Outline each uninfected red blood cell.
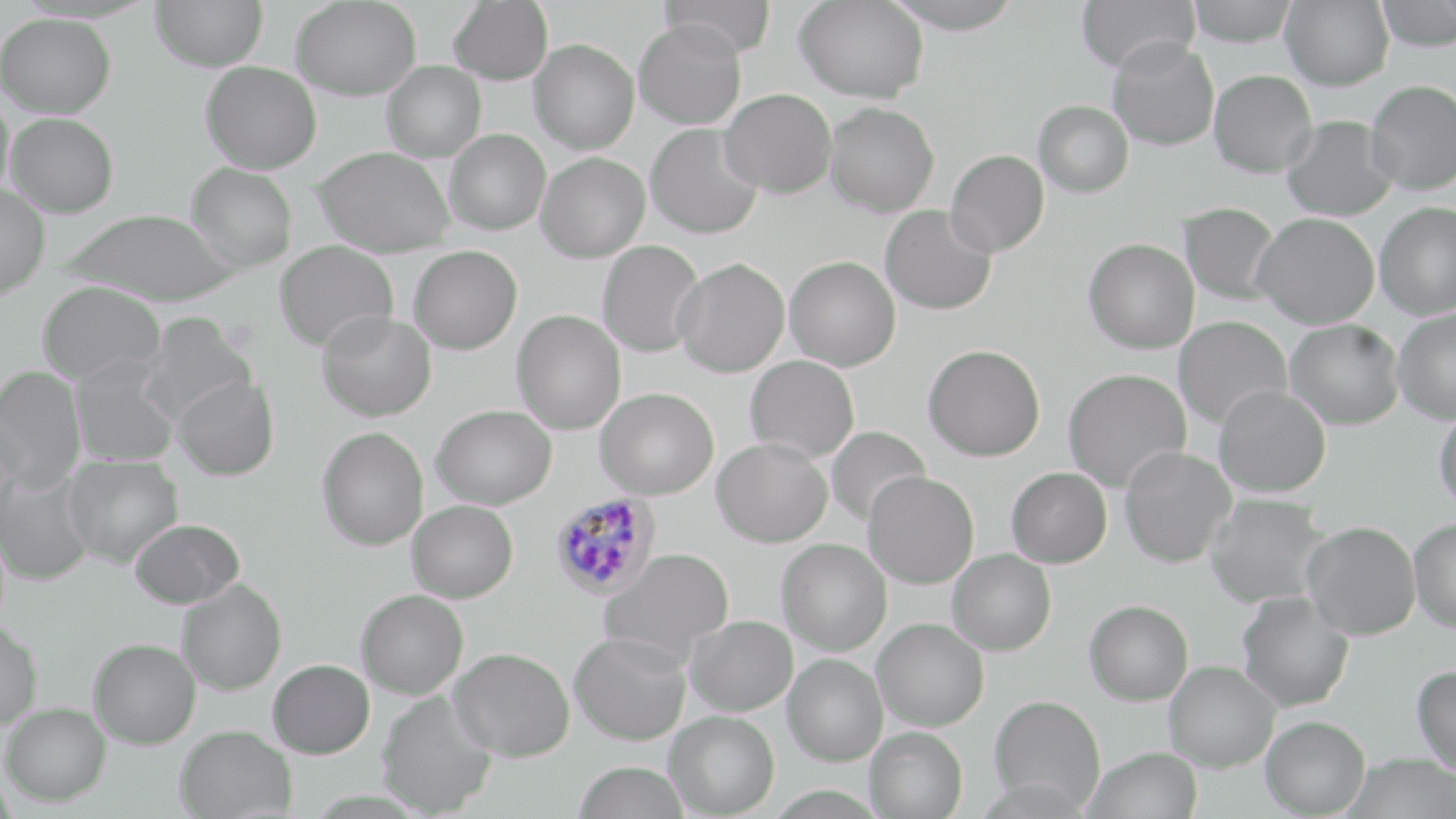
Approximate bounding boxes as (x1, y1, x2, y2) in pixels.
Uninfected red blood cells: (151, 0, 267, 72), (291, 0, 421, 101), (448, 0, 553, 85), (659, 0, 777, 60), (794, 0, 929, 103), (882, 0, 1024, 34), (1075, 0, 1200, 74), (1186, 0, 1298, 46), (1281, 0, 1393, 91), (1375, 0, 1455, 52), (0, 12, 116, 118), (633, 18, 747, 129), (1107, 37, 1220, 151), (528, 39, 640, 154), (382, 60, 486, 162), (201, 61, 322, 174), (1209, 70, 1317, 178), (1365, 79, 1456, 195), (720, 88, 837, 198), (0, 93, 14, 204), (1034, 100, 1133, 198), (824, 102, 939, 217), (5, 112, 119, 218), (1281, 116, 1399, 222), (645, 123, 764, 239), (445, 129, 550, 235), (312, 146, 455, 258), (945, 149, 1049, 257), (536, 151, 650, 263), (185, 162, 298, 271), (0, 183, 49, 299), (1374, 202, 1456, 320), (1179, 203, 1282, 305), (880, 205, 997, 315), (59, 208, 240, 306), (1252, 212, 1380, 328), (1083, 238, 1199, 353), (274, 239, 398, 352), (597, 240, 704, 358), (409, 245, 522, 354), (785, 256, 901, 370), (672, 257, 789, 377), (36, 280, 166, 385), (1392, 308, 1456, 424), (512, 310, 626, 435), (316, 311, 437, 422), (136, 312, 257, 424), (1173, 316, 1292, 430), (1284, 319, 1405, 430), (923, 344, 1045, 461), (745, 355, 859, 463), (70, 359, 180, 467), (0, 366, 87, 492), (1062, 368, 1191, 492), (172, 375, 280, 481), (1213, 384, 1331, 498), (594, 387, 719, 499), (432, 404, 556, 509), (1433, 404, 1456, 515), (317, 425, 429, 551), (824, 425, 931, 529), (711, 437, 833, 547), (1118, 446, 1236, 568), (63, 455, 183, 568), (1006, 467, 1112, 568), (0, 470, 94, 586), (863, 471, 979, 589), (1205, 494, 1332, 608), (407, 500, 518, 603), (129, 518, 244, 609), (1409, 518, 1456, 633), (1301, 521, 1420, 639), (777, 539, 892, 655), (599, 547, 735, 663), (947, 548, 1056, 655), (176, 579, 287, 696), (356, 589, 469, 699), (1236, 592, 1354, 712), (1084, 600, 1193, 705), (685, 615, 797, 716), (873, 617, 989, 731), (0, 620, 42, 730), (568, 632, 692, 745), (88, 638, 201, 749), (449, 647, 575, 761), (783, 654, 888, 766), (267, 659, 375, 759), (1164, 660, 1280, 772), (1411, 664, 1456, 775), (376, 690, 498, 817), (989, 694, 1106, 812), (2, 702, 111, 806), (664, 710, 779, 818), (1260, 715, 1370, 818), (174, 724, 296, 818), (865, 726, 968, 819), (1082, 747, 1202, 819), (1341, 753, 1455, 819), (573, 761, 689, 819).

Summary:
  - Plasmodium falciparum-infected red blood cell locations: (549, 491, 662, 601)
  - Slide-level diagnosis: Plasmodium falciparum
  - Magnification: 1000x
  - Preparation: thin blood film
  - Field of view: single
  - Image size: 1456×819 pixels
  - Stain: May-Grünwald-Giemsa
  - Modality: optical microscopy